Comment on the morphology of the erythrocytes.
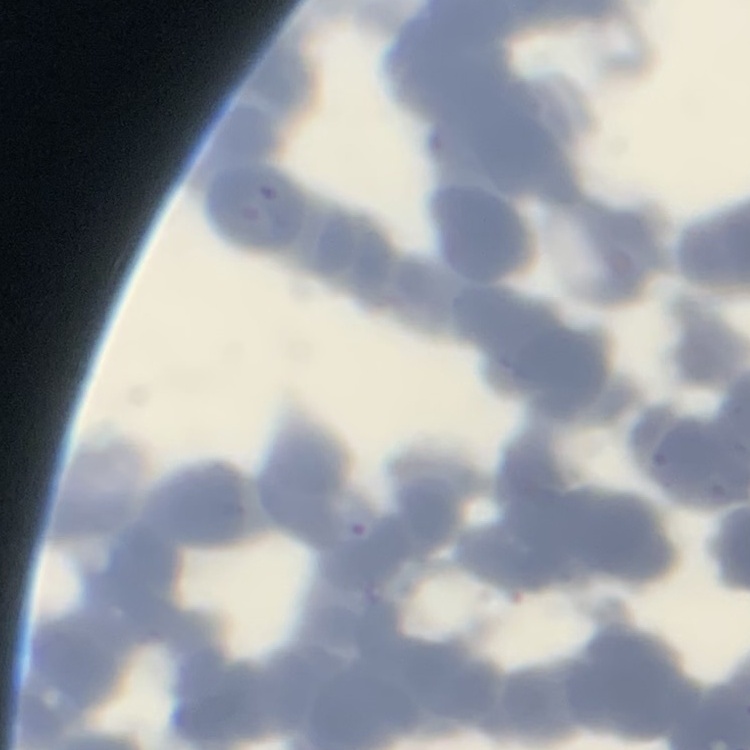

Rouleaux formation.

One tile cut from a larger photomicrograph. Thin peripheral smear. Stained with either Field's or Giemsa.